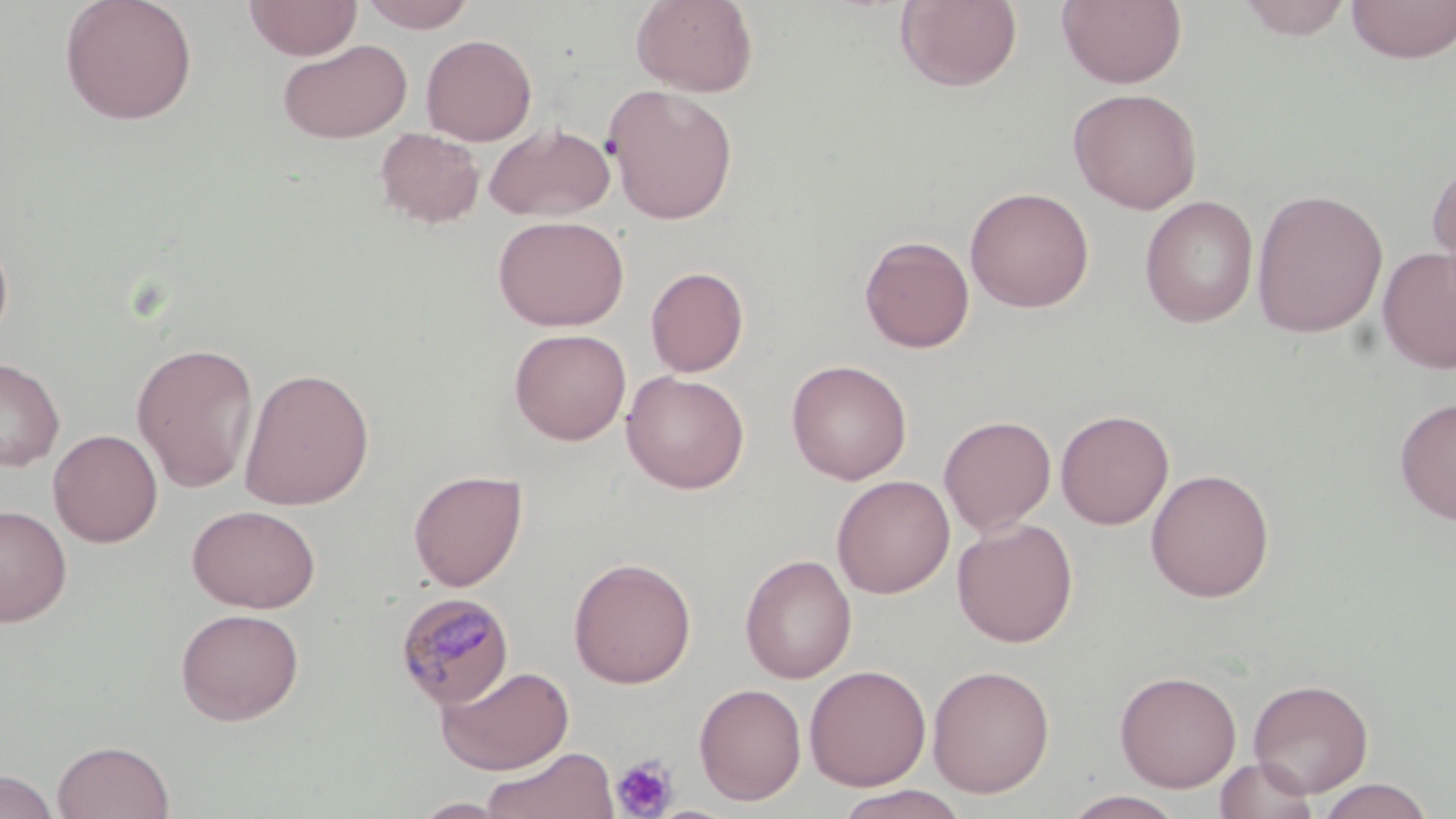

Summary:
  - Coordinate format: approximate bounding boxes as [x1, y1, x2, y2] in pixels
  - Uninfected red blood cell locations: [58, 0, 199, 125], [244, 0, 362, 60], [359, 0, 477, 32], [631, 0, 758, 97], [894, 0, 1022, 91], [1057, 0, 1187, 89], [1235, 0, 1355, 40], [1346, 0, 1456, 63], [421, 34, 537, 145], [277, 39, 412, 143], [603, 84, 739, 224], [1067, 87, 1203, 214], [484, 122, 616, 223], [375, 127, 486, 229], [1426, 157, 1456, 297], [964, 186, 1095, 313], [1251, 188, 1388, 338], [1139, 195, 1259, 328], [493, 215, 629, 331], [0, 228, 14, 350], [859, 234, 975, 353], [1376, 246, 1456, 375], [645, 266, 749, 377], [509, 328, 631, 445], [131, 341, 260, 492], [0, 357, 64, 471], [786, 359, 912, 484], [238, 367, 375, 511], [621, 370, 750, 494], [1394, 396, 1456, 525], [1055, 409, 1174, 530], [938, 415, 1056, 536], [48, 429, 163, 547], [1146, 468, 1275, 603], [408, 469, 528, 591], [831, 475, 955, 598], [0, 503, 72, 627], [186, 504, 321, 613], [952, 517, 1079, 647], [739, 553, 857, 683], [568, 556, 697, 689], [175, 607, 305, 725], [435, 664, 574, 775], [804, 664, 931, 790], [927, 664, 1055, 798], [1114, 670, 1242, 792], [1248, 678, 1373, 797], [694, 682, 807, 805], [52, 739, 175, 819], [480, 746, 619, 819], [1213, 756, 1320, 819], [0, 770, 59, 819], [1315, 778, 1436, 818], [832, 786, 969, 819], [1061, 790, 1187, 819], [409, 796, 518, 818]
  - Platelet locations: [611, 753, 680, 817]
  - Plasmodium malariae-infected red blood cell locations: [394, 592, 515, 710]
  - Slide-level diagnosis: Plasmodium malariae
  - Stain: May-Grünwald-Giemsa
  - Field of view: single
  - Image size: 1456×819 pixels
  - Magnification: 1000x
  - Modality: optical microscopy
  - Preparation: thin blood film